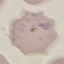
Result: no malaria parasites seen. Giemsa stain. Cell patch, automatically extracted from a larger field of view and resized to 64 × 64 pixels. Acquired by smartphone through the microscope eyepiece. Thin blood film.